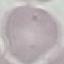
Malaria status: uninfected. Photographed with a smartphone camera at the microscope eyepiece. Thin smear of blood. Automatically extracted cell patch, resized to 64 × 64 pixels. Giemsa stain.